Report the malaria status of this cell.
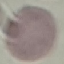

Uninfected.

Acquired by smartphone through the microscope eyepiece. Automatically extracted cell patch, resized to 64 × 64 pixels. Thin blood smear. Giemsa-stained preparation.